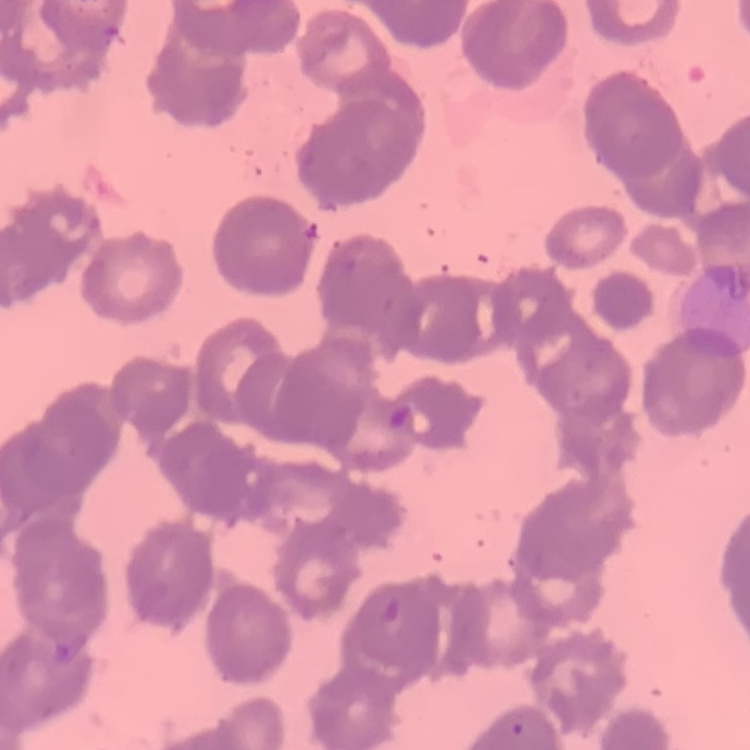
The red blood cells show rouleaux formation. Square crop of a larger photomicrograph. Stained with either Field's or Giemsa. Thin blood film.